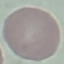

result = no malaria parasites seen
capture = smartphone camera at the microscope eyepiece
image type = automatically extracted cell patch, resized to 64 × 64 pixels
preparation = thin smear
stain = Giemsa